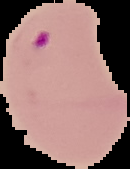

Summary:
  - Malaria status: parasitized
  - Image size: 130×169 pixels
  - Image type: cell region segmented out of the field of view; surrounding area masked to black
  - Preparation: thin blood film